Identify the cell.
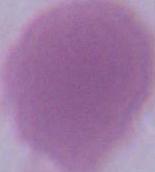

This is an erythrocyte.

Summary:
  - Magnification: 1000x
  - Modality: photomicrograph